Assess this cell for malaria.
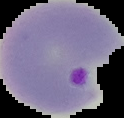
It is parasitized.

preparation = thin blood smear
image size = 124×118 pixels
image type = segmented cell region on a black background